Give the position of every leukocyte visible.
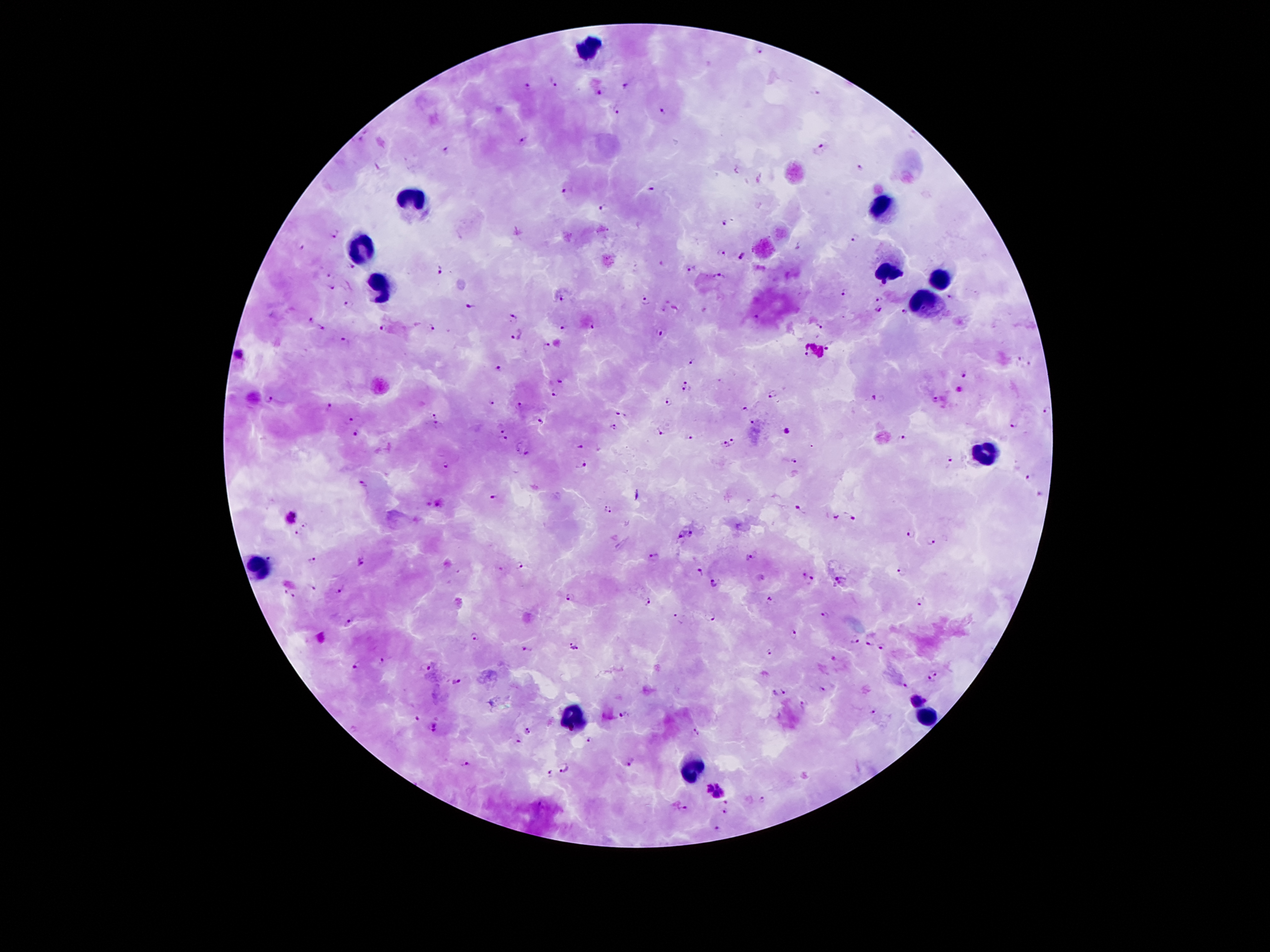
Approximate object centers, in pixels from the top-left corner.
Leukocytes: (x=592, y=47), (x=417, y=199), (x=884, y=206), (x=364, y=247), (x=889, y=269), (x=942, y=276), (x=378, y=285), (x=924, y=306), (x=987, y=451), (x=259, y=569), (x=926, y=714), (x=572, y=717), (x=691, y=770).

Plasmodium parasite locations: (x=762, y=50), (x=553, y=81), (x=625, y=84), (x=527, y=87), (x=598, y=92), (x=616, y=110), (x=663, y=112), (x=524, y=141), (x=823, y=146), (x=446, y=150), (x=860, y=166), (x=567, y=189), (x=651, y=189), (x=603, y=206), (x=723, y=222), (x=336, y=235), (x=855, y=237), (x=300, y=246), (x=721, y=253), (x=743, y=257), (x=353, y=267), (x=689, y=267), (x=439, y=268), (x=329, y=276), (x=719, y=276), (x=885, y=283), (x=332, y=287), (x=843, y=291), (x=563, y=296), (x=949, y=296), (x=878, y=297), (x=646, y=301), (x=347, y=305), (x=469, y=305), (x=879, y=307), (x=903, y=310), (x=513, y=316), (x=754, y=319), (x=309, y=320), (x=590, y=324), (x=563, y=325), (x=429, y=327), (x=821, y=327), (x=322, y=328), (x=381, y=330), (x=661, y=333), (x=518, y=334), (x=345, y=342), (x=828, y=344), (x=543, y=346), (x=240, y=356), (x=809, y=356), (x=1017, y=357), (x=691, y=361), (x=1029, y=365), (x=499, y=367), (x=966, y=372), (x=560, y=380), (x=687, y=385), (x=553, y=391), (x=773, y=394), (x=268, y=396), (x=875, y=396), (x=935, y=399), (x=493, y=402), (x=670, y=402), (x=331, y=404), (x=520, y=405), (x=745, y=408), (x=1047, y=412), (x=436, y=414), (x=622, y=416), (x=351, y=419), (x=541, y=421), (x=752, y=421), (x=436, y=423), (x=1015, y=424), (x=502, y=426), (x=611, y=427), (x=663, y=431), (x=787, y=431), (x=355, y=433), (x=900, y=437), (x=689, y=438), (x=504, y=440), (x=734, y=440), (x=726, y=444), (x=580, y=445), (x=524, y=452), (x=794, y=460), (x=948, y=461), (x=581, y=463), (x=444, y=465), (x=1030, y=476), (x=364, y=484), (x=1039, y=494), (x=493, y=497), (x=441, y=503), (x=798, y=506), (x=607, y=507), (x=850, y=516), (x=292, y=517), (x=835, y=517), (x=305, y=525), (x=692, y=533), (x=911, y=533), (x=295, y=535), (x=682, y=536), (x=933, y=542), (x=269, y=557), (x=654, y=557), (x=748, y=558), (x=312, y=560), (x=361, y=561), (x=519, y=566), (x=900, y=570), (x=700, y=571), (x=804, y=575), (x=840, y=580), (x=813, y=581), (x=714, y=582), (x=313, y=587), (x=284, y=590), (x=339, y=590), (x=569, y=596), (x=293, y=597), (x=769, y=598), (x=922, y=601), (x=649, y=603), (x=823, y=613), (x=678, y=618), (x=713, y=619), (x=351, y=621), (x=794, y=634), (x=320, y=637), (x=474, y=637), (x=856, y=640), (x=869, y=643), (x=574, y=646), (x=882, y=646), (x=524, y=649), (x=769, y=652), (x=383, y=659), (x=834, y=659), (x=356, y=665), (x=426, y=668), (x=936, y=669), (x=457, y=681), (x=930, y=682), (x=905, y=686), (x=822, y=688), (x=785, y=689), (x=775, y=692), (x=917, y=698), (x=804, y=705), (x=874, y=709), (x=624, y=716), (x=416, y=718), (x=435, y=725), (x=526, y=730), (x=697, y=732), (x=518, y=741), (x=588, y=741), (x=632, y=762), (x=465, y=764), (x=566, y=768), (x=551, y=772), (x=714, y=790), (x=763, y=799), (x=725, y=801), (x=682, y=807), (x=724, y=812), (x=717, y=828). Patient malaria status: infected with Plasmodium falciparum. Single field of view. Photographed through the microscope eyepiece with a smartphone camera. 100x magnification. Thick blood smear. Giemsa stain. Image is 1270×952 pixels.